Locate leukocytes (white blood cells).
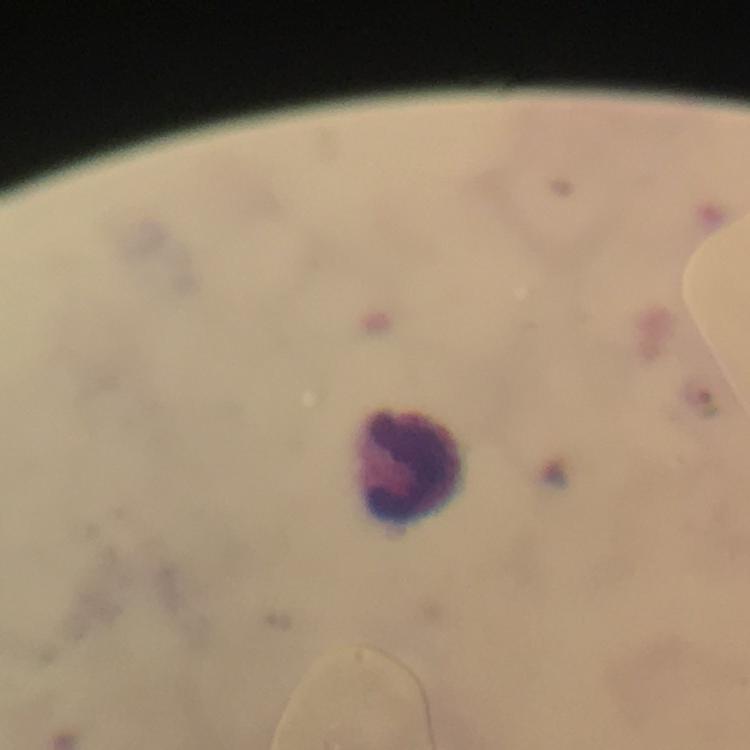
Approximate centers as [x, y] in pixels.
Leukocytes: [411, 466].

Malaria parasites: none detected. Immersion oil was used. Cropped region of a single field of view. Giemsa-stained preparation. Thick blood film. Image is 750×750 pixels. Smartphone photograph taken through a microscope. 100x magnification. From a diagnostic examination for malaria.